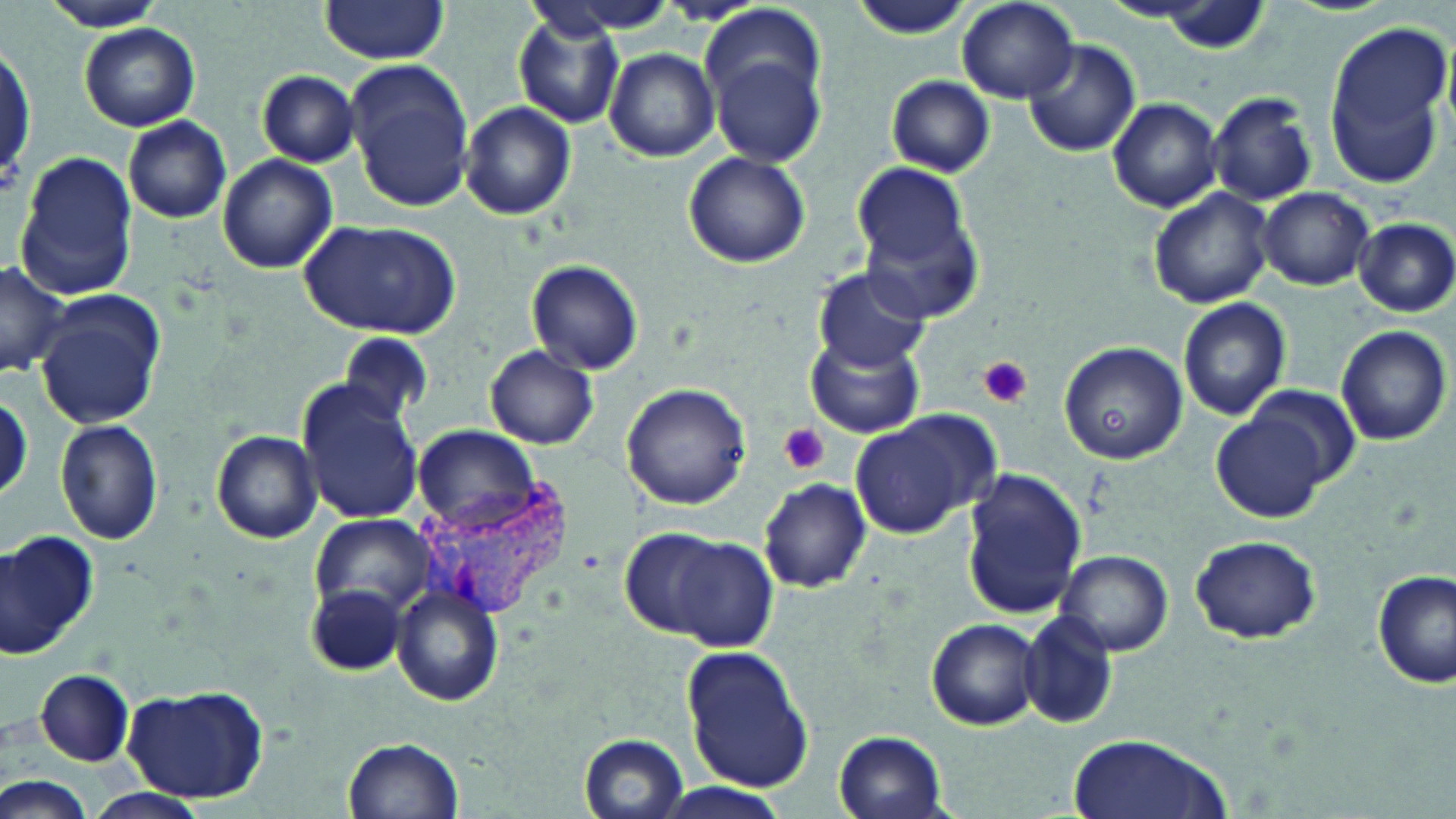
Summary:
  - Coordinate format: approximate bounding boxes as named x1/y1/x2/y2 corners in pixels
  - Uninfected red blood cell locations: (x1=36, y1=0, x2=168, y2=31), (x1=954, y1=0, x2=1078, y2=104), (x1=319, y1=1, x2=450, y2=63), (x1=849, y1=1, x2=974, y2=40), (x1=701, y1=7, x2=832, y2=167), (x1=513, y1=14, x2=625, y2=126), (x1=1322, y1=20, x2=1455, y2=186), (x1=81, y1=23, x2=200, y2=132), (x1=1022, y1=36, x2=1140, y2=158), (x1=2, y1=40, x2=35, y2=200), (x1=605, y1=49, x2=719, y2=163), (x1=344, y1=60, x2=475, y2=212), (x1=257, y1=70, x2=360, y2=167), (x1=886, y1=75, x2=994, y2=177), (x1=1207, y1=90, x2=1319, y2=207), (x1=1106, y1=96, x2=1222, y2=211), (x1=459, y1=101, x2=577, y2=221), (x1=123, y1=116, x2=231, y2=225), (x1=683, y1=151, x2=810, y2=269), (x1=15, y1=152, x2=139, y2=299), (x1=217, y1=154, x2=338, y2=274), (x1=849, y1=161, x2=974, y2=271), (x1=1149, y1=187, x2=1275, y2=310), (x1=1257, y1=187, x2=1373, y2=290), (x1=853, y1=188, x2=987, y2=327), (x1=1353, y1=217, x2=1455, y2=317), (x1=301, y1=218, x2=460, y2=340), (x1=526, y1=259, x2=644, y2=376), (x1=0, y1=262, x2=68, y2=378), (x1=814, y1=268, x2=929, y2=371), (x1=32, y1=290, x2=165, y2=431), (x1=1177, y1=297, x2=1291, y2=421), (x1=1334, y1=324, x2=1451, y2=445), (x1=807, y1=329, x2=924, y2=437), (x1=339, y1=331, x2=429, y2=425), (x1=1059, y1=341, x2=1186, y2=462), (x1=485, y1=346, x2=598, y2=449), (x1=298, y1=382, x2=424, y2=525), (x1=622, y1=383, x2=751, y2=509), (x1=1244, y1=385, x2=1359, y2=487), (x1=0, y1=395, x2=30, y2=503), (x1=1212, y1=411, x2=1332, y2=523), (x1=849, y1=415, x2=986, y2=538), (x1=55, y1=419, x2=165, y2=544), (x1=412, y1=426, x2=538, y2=529), (x1=211, y1=429, x2=322, y2=544), (x1=962, y1=468, x2=1090, y2=621), (x1=758, y1=478, x2=872, y2=593), (x1=311, y1=514, x2=436, y2=616), (x1=618, y1=527, x2=739, y2=636), (x1=0, y1=529, x2=97, y2=653), (x1=666, y1=536, x2=779, y2=648), (x1=1189, y1=536, x2=1320, y2=643), (x1=1056, y1=550, x2=1173, y2=655), (x1=1372, y1=569, x2=1454, y2=689), (x1=392, y1=585, x2=503, y2=707), (x1=302, y1=586, x2=403, y2=676), (x1=1019, y1=612, x2=1121, y2=729), (x1=925, y1=617, x2=1043, y2=730), (x1=681, y1=643, x2=814, y2=794), (x1=33, y1=669, x2=136, y2=767), (x1=122, y1=683, x2=269, y2=805), (x1=834, y1=731, x2=948, y2=817), (x1=1067, y1=732, x2=1229, y2=819), (x1=578, y1=733, x2=690, y2=818), (x1=343, y1=737, x2=464, y2=819), (x1=2, y1=775, x2=89, y2=819), (x1=649, y1=782, x2=794, y2=819), (x1=79, y1=787, x2=210, y2=819)
  - Platelet locations: (x1=978, y1=356, x2=1033, y2=409), (x1=779, y1=425, x2=830, y2=475)
  - Plasmodium vivax-infected red blood cell locations: (x1=410, y1=480, x2=575, y2=618)
  - Slide-level diagnosis: Plasmodium vivax
  - Preparation: thin blood smear
  - Modality: optical microscopy
  - Stain: May-Grünwald-Giemsa
  - Image size: 1456×819 pixels
  - Field of view: one of a larger specimen
  - Magnification: 1000x